Assess the morphology of the erythrocytes.
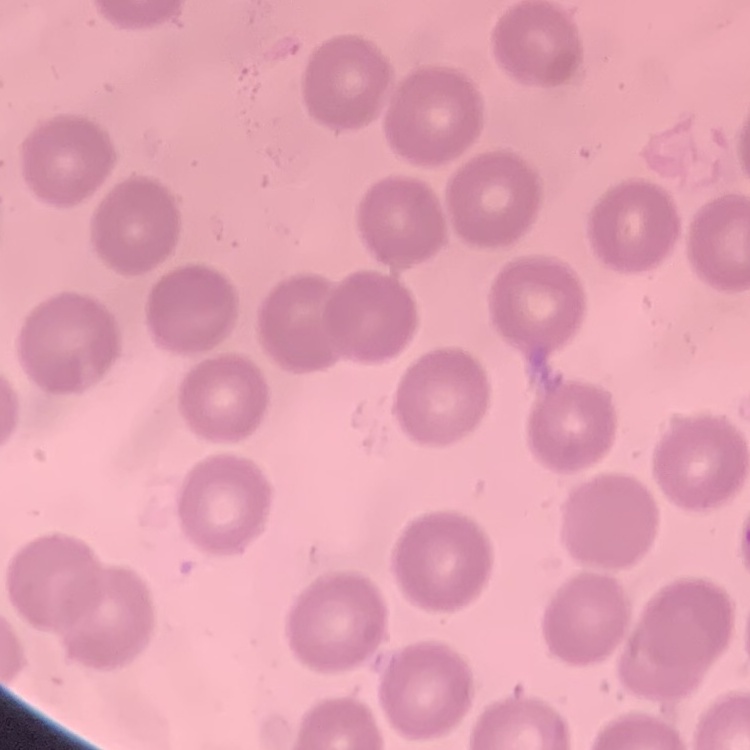
They show no rouleaux formation.

image_type: one tile cut from a larger photomicrograph
stain: Field's or Giemsa
preparation: thin blood smear